Give the extent of all Plasmodium falciparum-infected red blood cells.
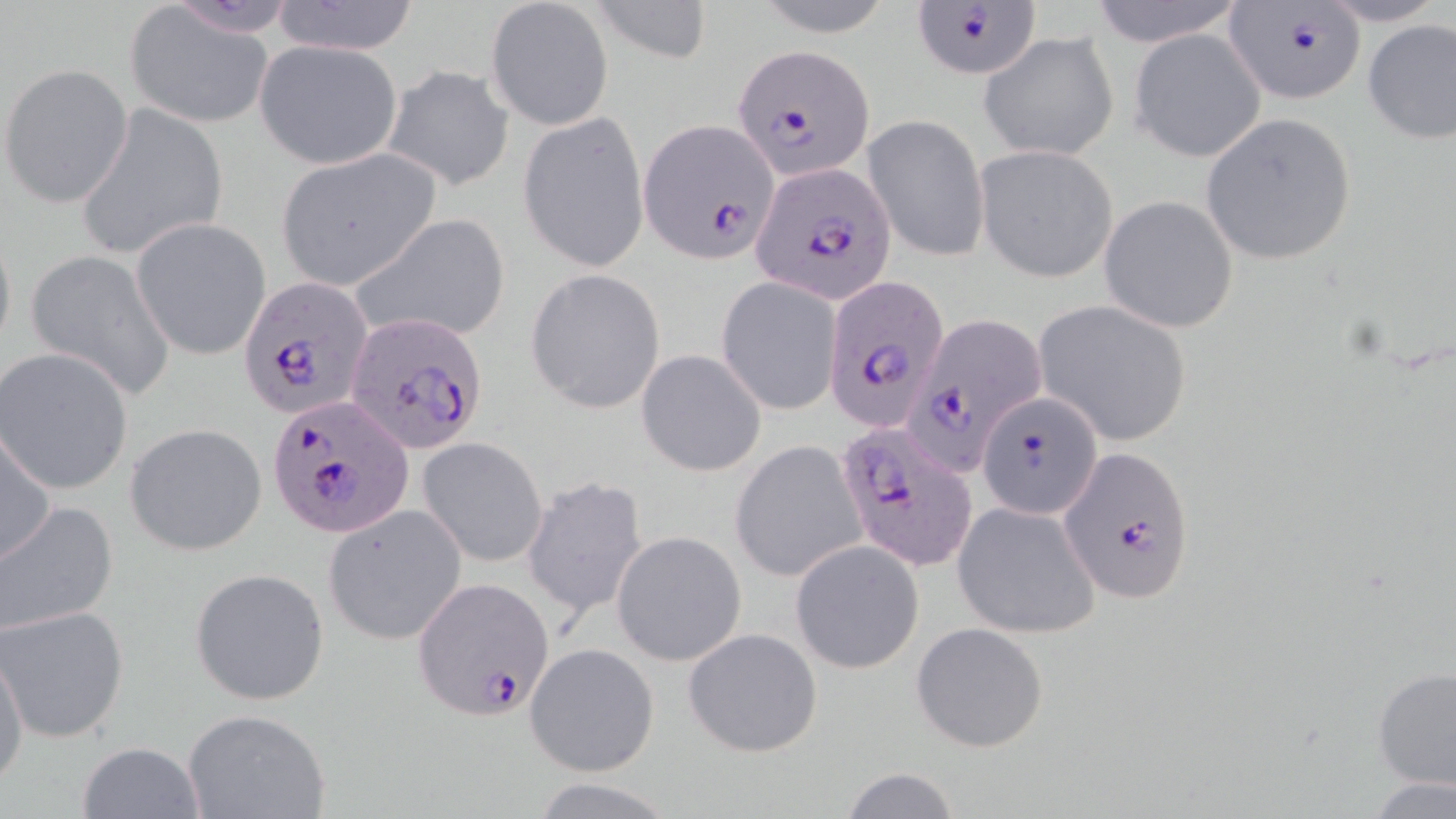
Approximate bounding boxes as [x1, y1, x2, y2] in pixels.
Plasmodium falciparum-infected red blood cells: [908, 2, 1044, 81], [1222, 3, 1364, 105], [732, 44, 873, 179], [641, 119, 777, 263], [752, 162, 894, 301], [823, 273, 946, 434], [240, 277, 371, 418], [346, 309, 490, 460], [904, 311, 1047, 473], [977, 393, 1103, 520], [267, 395, 414, 539], [834, 420, 977, 573], [1057, 445, 1196, 604], [415, 577, 552, 721].

Uninfected red blood cell locations: [274, 0, 420, 56], [486, 0, 613, 131], [592, 0, 712, 66], [1084, 0, 1249, 46], [1312, 0, 1448, 27], [749, 1, 898, 36], [126, 8, 274, 127], [1361, 18, 1456, 144], [1129, 28, 1267, 163], [978, 30, 1119, 162], [252, 39, 404, 169], [382, 64, 515, 192], [2, 65, 133, 208], [73, 101, 228, 261], [1200, 111, 1358, 267], [518, 112, 648, 271], [865, 115, 988, 262], [976, 145, 1118, 282], [279, 148, 436, 286], [1098, 194, 1239, 333], [349, 212, 511, 346], [131, 217, 274, 361], [0, 223, 16, 364], [22, 250, 175, 402], [525, 267, 666, 414], [717, 276, 843, 416], [1034, 300, 1192, 447], [1, 347, 134, 495], [635, 348, 767, 477], [123, 422, 267, 557], [1, 424, 55, 569], [418, 433, 549, 568], [732, 440, 866, 583], [520, 474, 649, 621], [953, 501, 1100, 639], [0, 502, 119, 636], [324, 507, 467, 644], [612, 531, 747, 666], [791, 541, 924, 674], [190, 567, 330, 707], [2, 608, 129, 742], [911, 622, 1048, 753], [683, 627, 822, 756], [1, 642, 27, 789], [523, 642, 660, 778], [1372, 664, 1455, 794], [179, 707, 335, 819], [75, 741, 205, 818], [833, 767, 965, 819], [530, 777, 677, 817], [1367, 777, 1455, 818]. Slide-level diagnosis: Plasmodium falciparum. Image is 1456×819 pixels. One field of a larger specimen. May-Grünwald-Giemsa-stained preparation. 1000x magnification. Light microscopy. Thin blood smear.